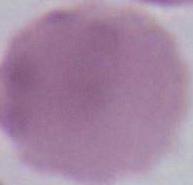 1000x magnification. Micrograph. An erythrocyte is shown.